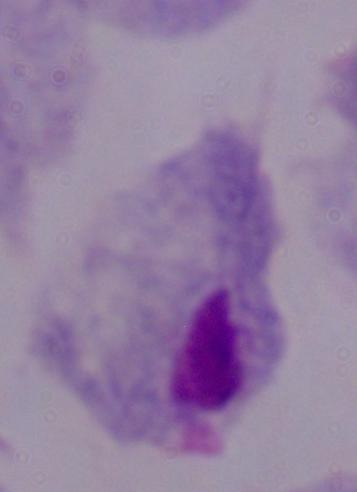
Summary:
  - Identification: trichomonad
  - Magnification: 1000x
  - Modality: photomicrograph